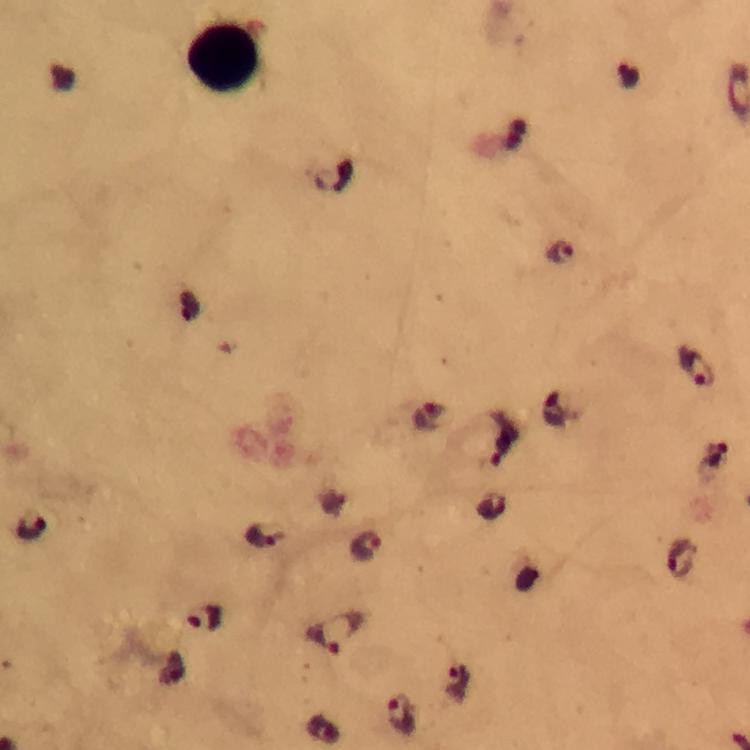

immersion oil = used
Plasmodium parasite locations = approximate centers as {x, y} in pixels: {628, 77}, {332, 178}, {559, 254}, {696, 367}, {555, 410}, {426, 421}, {503, 438}, {715, 455}, {33, 528}, {265, 537}, {368, 547}, {682, 561}, {206, 618}, {337, 632}, {459, 685}, {402, 714}
image size = 750×750 pixels
magnification = 100x
capture = smartphone mounted on the microscope
preparation = thick blood film
leukocyte locations = approximate centers as {x, y} in pixels: {224, 56}
cropped from = one field of view
stain = Giemsa
context = from a malaria diagnostic workup